State which parasite is depicted.
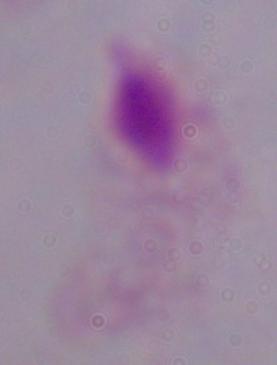

A trichomonad.

{
  "modality": "photomicrograph",
  "magnification": "1000x"
}